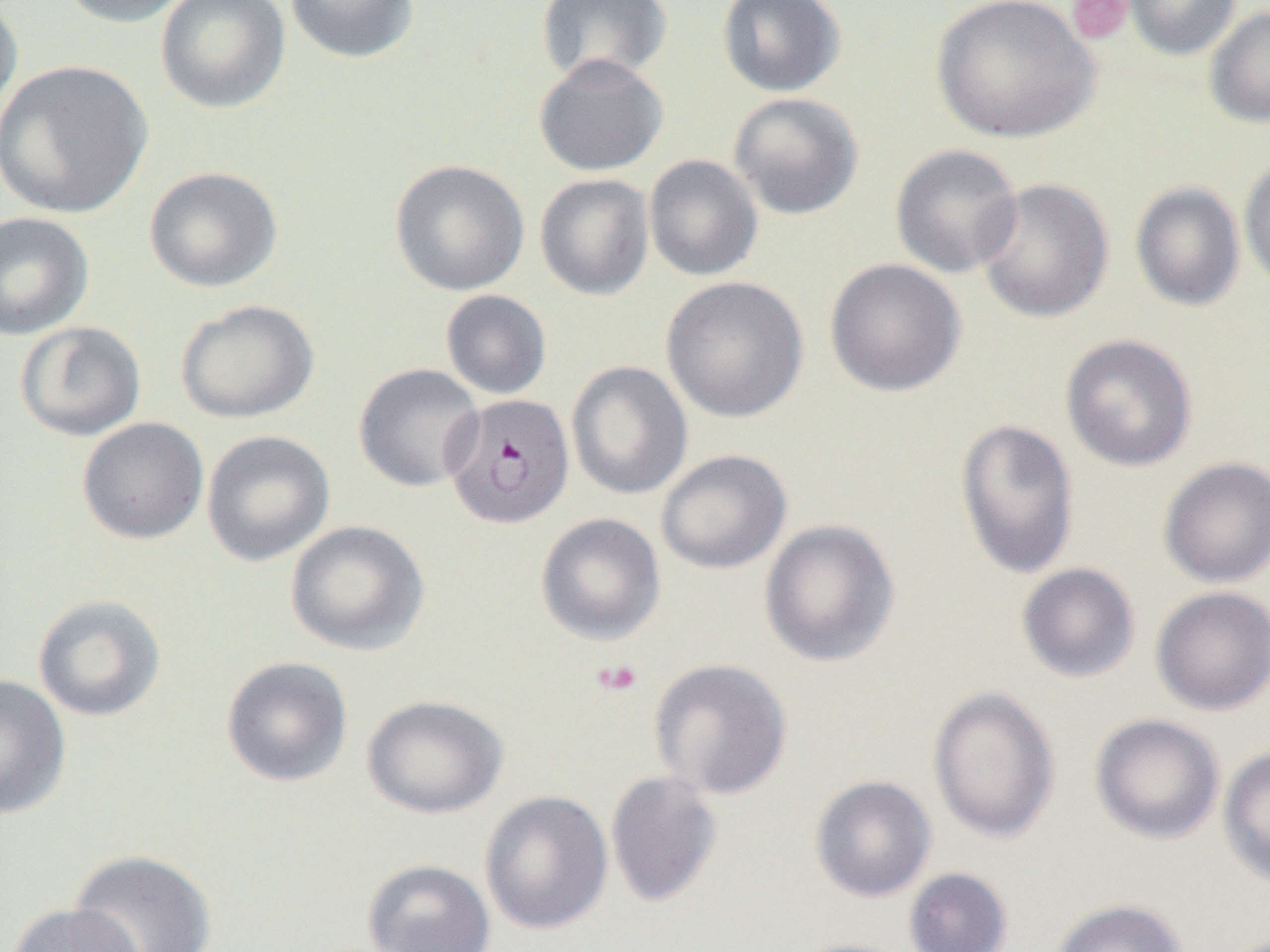

{
  "slide_level_diagnosis": "Plasmodium falciparum",
  "platelet_locations": "approximate bounding boxes as named x1/y1/x2/y2 corners in pixels: (x1=1066, y1=0, x2=1133, y2=45), (x1=592, y1=659, x2=643, y2=696)",
  "uninfected_red_blood_cell_locations": "approximate bounding boxes as named x1/y1/x2/y2 corners in pixels: (x1=55, y1=0, x2=195, y2=27), (x1=155, y1=0, x2=290, y2=114), (x1=284, y1=0, x2=420, y2=63), (x1=716, y1=0, x2=846, y2=98), (x1=931, y1=0, x2=1101, y2=144), (x1=1123, y1=0, x2=1241, y2=60), (x1=0, y1=1, x2=23, y2=127), (x1=535, y1=1, x2=673, y2=86), (x1=1205, y1=7, x2=1270, y2=127), (x1=533, y1=54, x2=669, y2=177), (x1=0, y1=59, x2=153, y2=218), (x1=727, y1=92, x2=864, y2=220), (x1=890, y1=144, x2=1024, y2=278), (x1=643, y1=154, x2=763, y2=282), (x1=1238, y1=156, x2=1270, y2=295), (x1=389, y1=159, x2=530, y2=296), (x1=143, y1=166, x2=283, y2=292), (x1=534, y1=173, x2=654, y2=301), (x1=974, y1=177, x2=1114, y2=323), (x1=1130, y1=182, x2=1246, y2=311), (x1=0, y1=211, x2=94, y2=340), (x1=824, y1=259, x2=966, y2=397), (x1=661, y1=276, x2=809, y2=424), (x1=440, y1=290, x2=552, y2=400), (x1=175, y1=299, x2=319, y2=424), (x1=14, y1=321, x2=147, y2=441), (x1=1060, y1=334, x2=1197, y2=472), (x1=566, y1=360, x2=693, y2=500), (x1=353, y1=363, x2=485, y2=492), (x1=76, y1=417, x2=209, y2=544), (x1=955, y1=418, x2=1080, y2=579), (x1=201, y1=430, x2=335, y2=566), (x1=656, y1=449, x2=792, y2=574), (x1=1158, y1=456, x2=1270, y2=588), (x1=535, y1=512, x2=666, y2=645), (x1=759, y1=518, x2=901, y2=667), (x1=285, y1=520, x2=430, y2=656), (x1=1016, y1=562, x2=1140, y2=683), (x1=1151, y1=586, x2=1270, y2=715), (x1=32, y1=594, x2=167, y2=722), (x1=221, y1=655, x2=353, y2=787), (x1=649, y1=657, x2=794, y2=800), (x1=0, y1=673, x2=71, y2=819), (x1=927, y1=685, x2=1061, y2=842), (x1=361, y1=694, x2=508, y2=818), (x1=1090, y1=713, x2=1226, y2=844), (x1=1218, y1=745, x2=1270, y2=890), (x1=605, y1=770, x2=723, y2=908), (x1=809, y1=775, x2=936, y2=902), (x1=479, y1=789, x2=612, y2=934), (x1=68, y1=848, x2=217, y2=952), (x1=361, y1=858, x2=496, y2=952), (x1=904, y1=867, x2=1013, y2=951), (x1=1048, y1=898, x2=1187, y2=952), (x1=6, y1=902, x2=146, y2=952), (x1=784, y1=937, x2=916, y2=952)",
  "magnification": "1000x",
  "field_of_view": "one of a larger specimen",
  "image_size": "1270×952 pixels",
  "plasmodium_falciparum_infected_red_blood_cell_locations": "approximate bounding boxes as named x1/y1/x2/y2 corners in pixels: (x1=443, y1=394, x2=575, y2=529)",
  "preparation": "thin blood smear",
  "modality": "optical microscopy"
}